Identify the parasite.
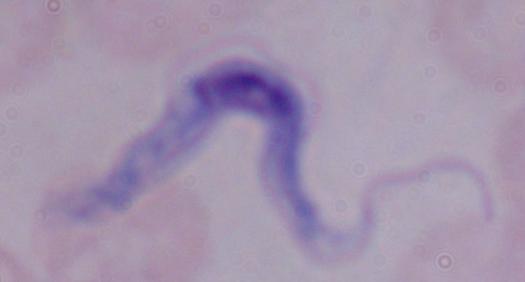

A trypanosome.

Summary:
  - Magnification: 1000x
  - Modality: micrograph